Locate every blood parasite and identify its species.
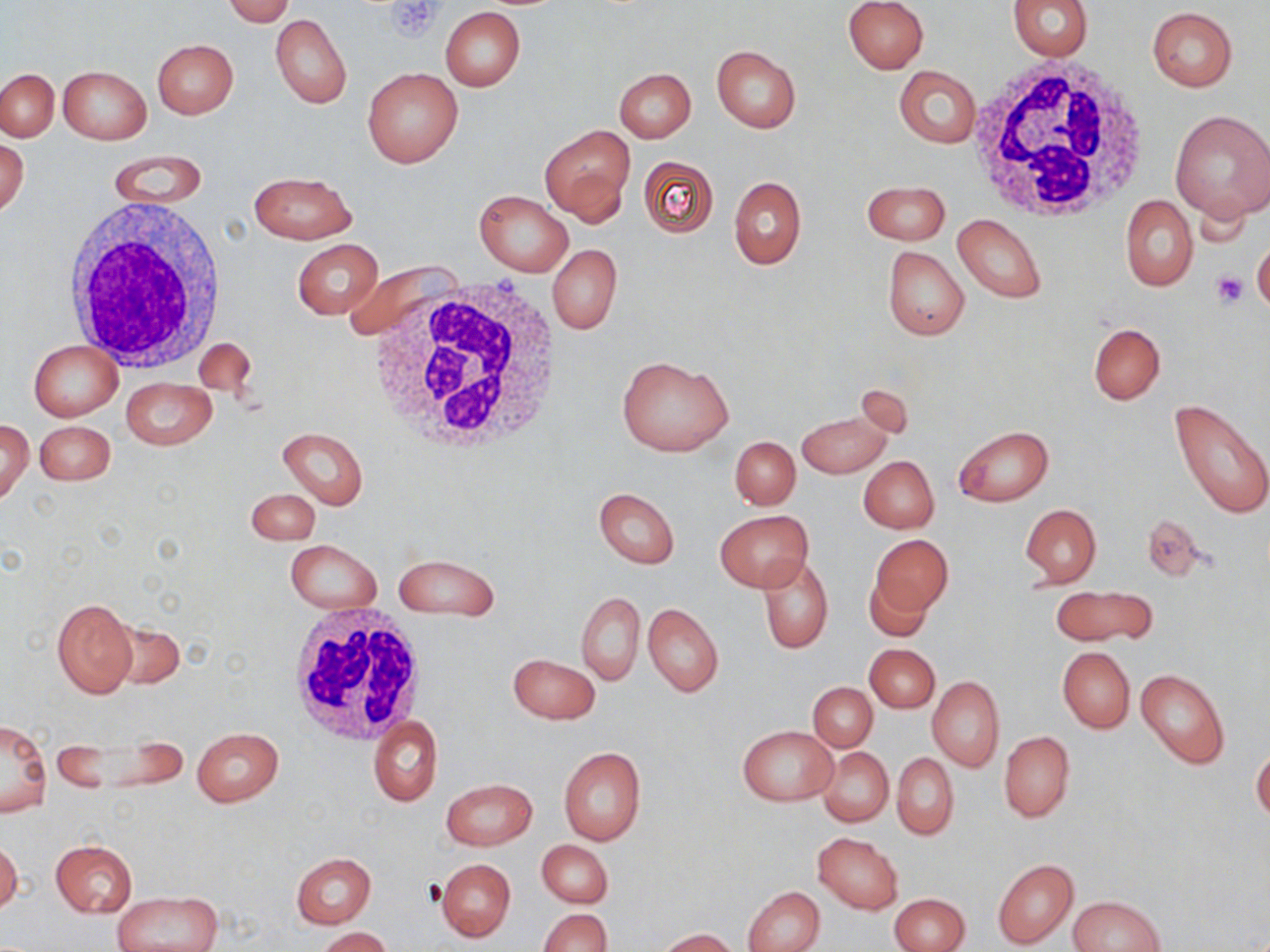

No blood parasites observed.

Approximate bounding boxes as [x1, y1, x2, y2] in pixels. White blood cell locations: [965, 55, 1155, 224], [63, 196, 228, 375], [371, 274, 565, 456], [284, 607, 426, 744]. Uninfected red blood cell locations: [222, 0, 295, 25], [842, 0, 928, 74], [1008, 0, 1094, 60], [1147, 6, 1237, 91], [441, 7, 525, 91], [270, 14, 351, 108], [152, 38, 238, 119], [711, 45, 802, 132], [58, 64, 152, 144], [893, 65, 981, 148], [362, 67, 462, 168], [614, 68, 696, 142], [1, 69, 58, 141], [1168, 108, 1270, 224], [541, 125, 635, 223], [0, 135, 29, 220], [104, 150, 208, 210], [637, 154, 719, 238], [249, 171, 357, 243], [729, 176, 806, 269], [860, 180, 951, 246], [474, 190, 573, 276], [1120, 196, 1196, 291], [953, 214, 1046, 304], [293, 239, 381, 320], [1252, 239, 1270, 316], [547, 244, 621, 336], [882, 245, 970, 341], [339, 260, 453, 343], [1088, 322, 1165, 405], [193, 338, 257, 400], [29, 340, 123, 420], [617, 356, 733, 457], [121, 377, 215, 449], [1170, 399, 1269, 520], [796, 409, 892, 478], [0, 419, 32, 505], [36, 421, 114, 485], [953, 425, 1053, 506], [276, 427, 368, 509], [730, 436, 799, 510], [859, 456, 939, 534], [594, 487, 679, 568], [247, 489, 320, 545], [1019, 503, 1102, 587], [715, 510, 812, 593], [1140, 513, 1212, 582], [870, 534, 952, 620], [286, 540, 381, 614], [395, 553, 501, 619], [758, 556, 832, 653], [862, 571, 935, 643], [1051, 586, 1156, 646], [576, 591, 644, 685], [52, 598, 138, 698], [643, 603, 723, 697], [107, 619, 185, 691], [865, 644, 939, 712], [1058, 647, 1135, 733], [508, 654, 601, 723], [1136, 669, 1230, 769], [927, 677, 1003, 771], [808, 683, 877, 752], [369, 716, 443, 806], [1, 722, 52, 818], [737, 726, 837, 805], [191, 727, 284, 806], [999, 731, 1075, 822], [819, 747, 893, 826], [558, 748, 647, 845], [1251, 748, 1270, 821], [892, 754, 959, 840], [441, 778, 537, 850], [813, 832, 903, 914], [0, 840, 22, 916], [49, 840, 137, 917], [537, 840, 612, 908], [291, 852, 376, 928], [437, 859, 515, 942], [993, 859, 1078, 949], [744, 887, 824, 952], [111, 891, 224, 952], [890, 893, 970, 952], [1069, 895, 1164, 951], [538, 908, 611, 952], [316, 927, 392, 952], [657, 928, 740, 952]. Platelet locations: [384, 1, 444, 39], [1211, 271, 1247, 308]. Slide-level diagnosis: no evidence of blood parasites. One field of a larger specimen. Thin blood film. 1000x magnification. Light microscopy. Image is 1270×952 pixels. May-Grünwald-Giemsa stain.